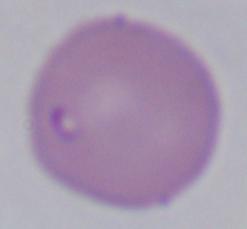

1000x magnification. Photomicrograph. A Babesia parasite is seen.